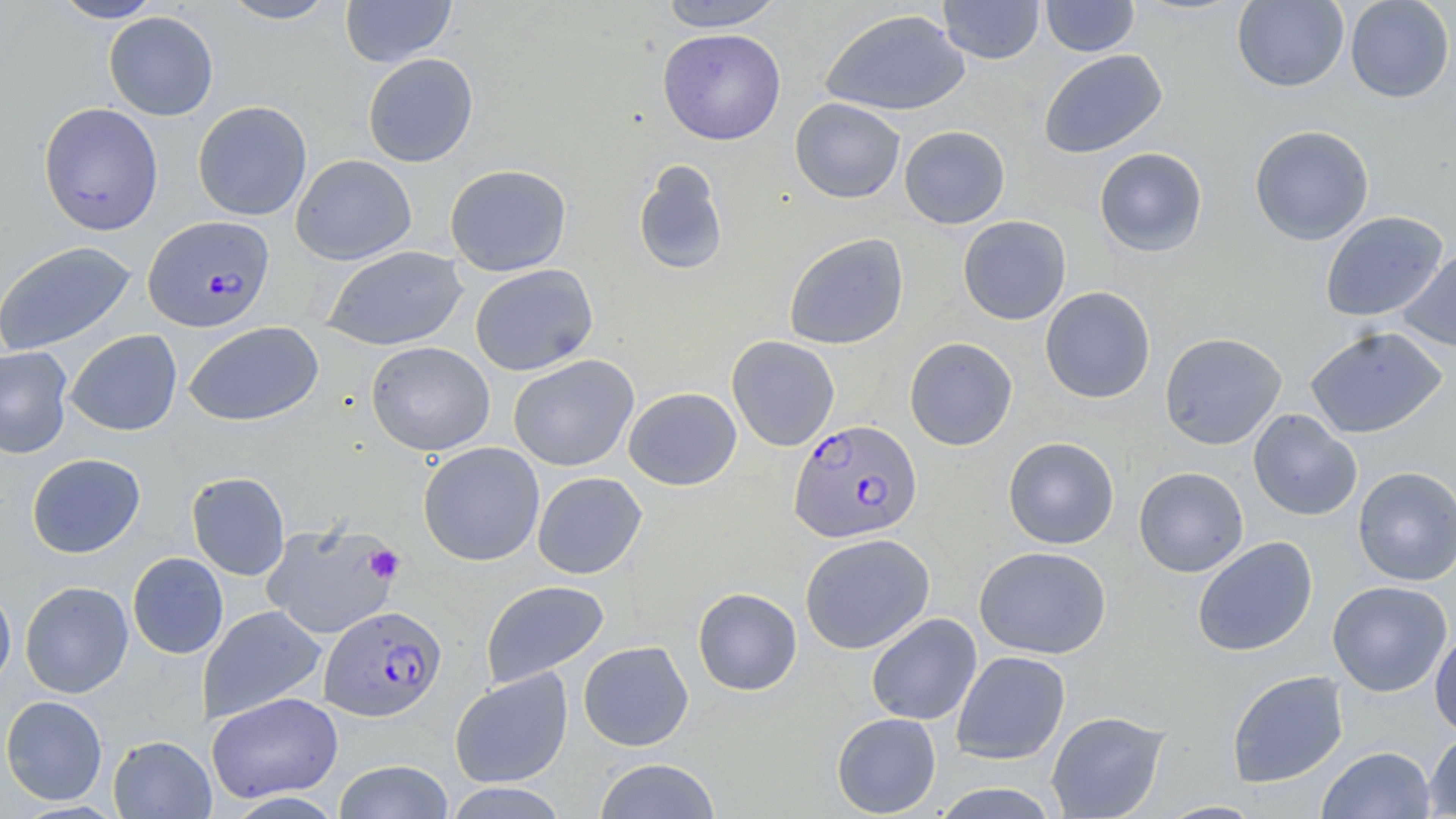
Summary:
  - Coordinate format: approximate bounding boxes as (x1,y1)-(x2,y2) corner pairs in pixels
  - Platelet locations: (365,545)-(404,584)
  - Uninfected red blood cell locations: (50,0)-(165,22), (218,0)-(340,24), (340,0)-(456,67), (658,0)-(786,31), (938,0)-(1044,64), (1041,0)-(1140,57), (1345,0)-(1454,103), (1232,1)-(1348,92), (819,9)-(970,116), (103,11)-(219,121), (658,28)-(786,145), (1038,49)-(1168,159), (362,53)-(479,167), (790,97)-(906,203), (192,100)-(312,221), (38,102)-(164,236), (1249,124)-(1374,246), (899,125)-(1011,229), (1093,147)-(1208,257), (290,154)-(416,265), (632,160)-(729,277), (444,164)-(572,277), (1320,211)-(1448,322), (958,215)-(1071,325), (783,233)-(909,350), (0,240)-(137,356), (321,245)-(469,351), (1398,247)-(1456,353), (469,264)-(598,376), (1040,286)-(1156,404), (184,321)-(324,426), (1305,326)-(1448,438), (65,329)-(182,436), (1160,332)-(1287,450), (727,335)-(840,451), (904,337)-(1018,451), (366,341)-(495,456), (0,346)-(73,458), (508,354)-(639,472), (624,387)-(741,490), (1248,409)-(1362,521), (1003,437)-(1120,549), (418,441)-(545,566), (27,452)-(146,558), (1133,466)-(1249,577), (1353,467)-(1455,585), (186,472)-(290,580), (532,472)-(647,579), (262,520)-(402,640), (799,533)-(935,654), (1192,536)-(1318,657), (974,546)-(1111,659), (127,552)-(229,659), (19,580)-(133,698), (481,580)-(610,688), (1327,580)-(1453,697), (0,582)-(17,694), (693,587)-(802,695), (198,605)-(327,723), (866,613)-(982,726), (1430,628)-(1456,738), (578,640)-(693,751), (951,651)-(1070,765), (449,668)-(574,788), (1226,670)-(1348,787), (206,692)-(343,803), (1,695)-(107,805), (1046,710)-(1169,819), (831,712)-(941,817), (1424,730)-(1456,818), (108,735)-(216,818), (1317,746)-(1435,819), (593,758)-(722,819), (333,760)-(454,819), (441,782)-(570,818), (930,783)-(1062,818), (1157,801)-(1264,819)
  - Plasmodium falciparum-infected red blood cell locations: (143,215)-(275,332), (788,418)-(923,543), (319,605)-(446,721)
  - Slide-level diagnosis: Plasmodium falciparum
  - Modality: optical microscopy
  - Preparation: thin blood film
  - Stain: May-Grünwald-Giemsa
  - Magnification: 1000x
  - Field of view: single
  - Image size: 1456×819 pixels